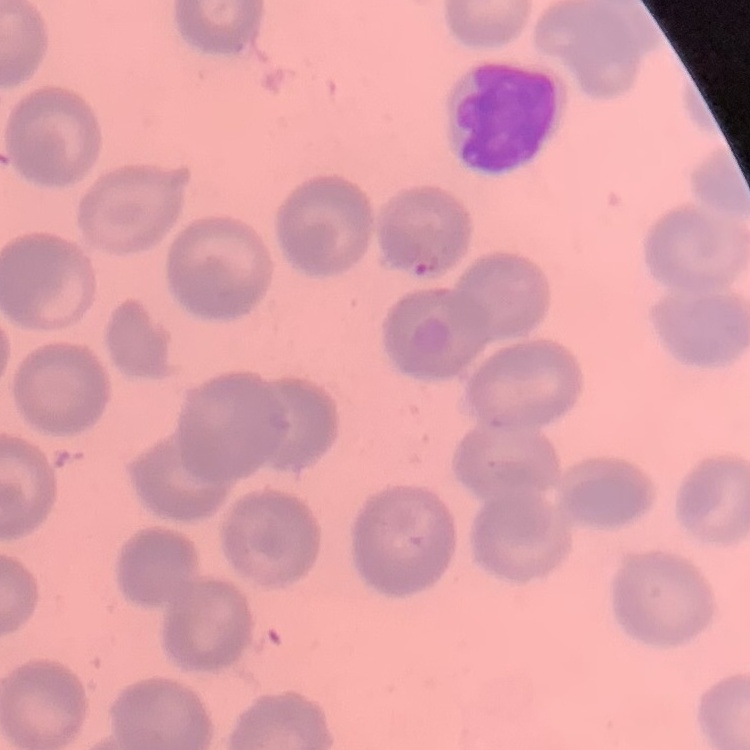

The red blood cells exhibit no rouleaux formation. Thin blood film. Field's or Giemsa stain. One tile cut from a larger photomicrograph.